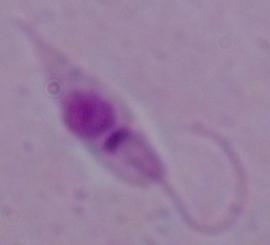

Summary:
  - Identification: Leishmania
  - Magnification: 1000x
  - Modality: photomicrograph